Assess this cell for malaria.
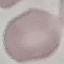
Uninfected.

stain: Giemsa
capture: smartphone through the microscope eyepiece
preparation: thin smear
image_type: cell patch, automatically extracted from a larger field of view and resized to 64 × 64 pixels